Classify this cell by malaria status.
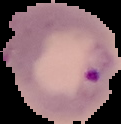

It is parasitized.

Summary:
  - Image size: 121×124 pixels
  - Preparation: thin blood smear
  - Image type: segmented cell region with the area outside set to black